Give the extent of all Plasmodium ovale-infected red blood cells.
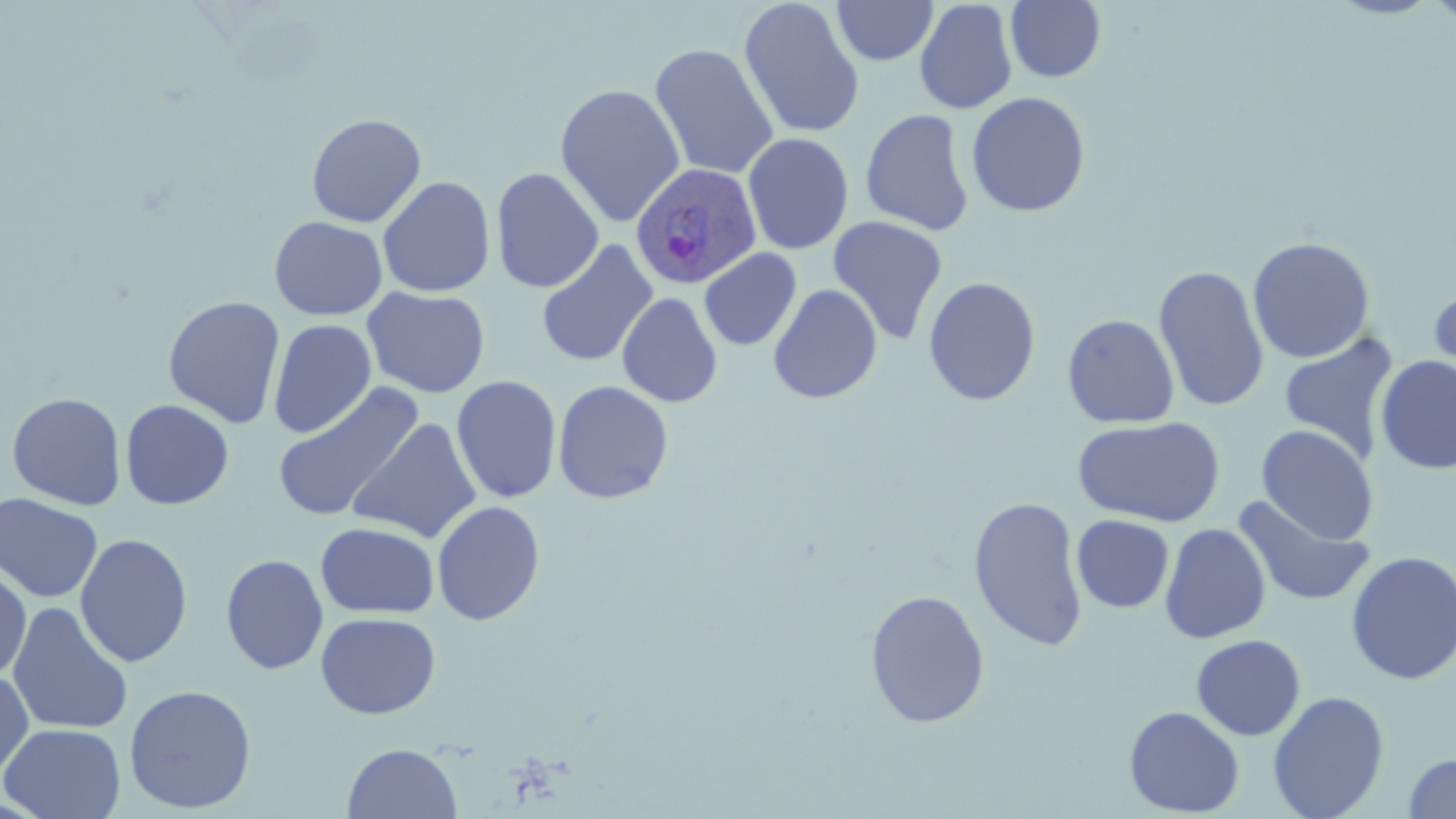

Approximate bounding boxes as (x1, y1, x2, y2) in pixels.
Plasmodium ovale-infected red blood cells: (629, 162, 763, 289).

{
  "slide_level_diagnosis": "Plasmodium ovale",
  "stain": "May-Grünwald-Giemsa",
  "field_of_view": "one of a larger specimen",
  "modality": "light microscopy",
  "image_size": "1456×819 pixels",
  "preparation": "thin blood smear",
  "magnification": "1000x",
  "uninfected_red_blood_cell_locations": "approximate bounding boxes as (x1, y1, x2, y2) in pixels: (739, 0, 865, 139), (831, 0, 938, 66), (914, 0, 1019, 115), (1328, 0, 1444, 19), (1426, 0, 1456, 28), (1004, 1, 1107, 83), (649, 43, 779, 180), (554, 83, 686, 227), (966, 91, 1090, 218), (860, 109, 975, 236), (306, 113, 427, 228), (741, 132, 854, 255), (490, 167, 604, 293), (377, 176, 496, 298), (269, 215, 388, 321), (828, 215, 949, 345), (1246, 236, 1376, 364), (536, 239, 658, 368), (699, 248, 802, 351), (1153, 264, 1270, 413), (923, 276, 1041, 406), (1426, 280, 1456, 400), (767, 283, 883, 404), (362, 286, 490, 398), (617, 292, 723, 408), (162, 295, 286, 429), (1062, 313, 1180, 429), (268, 318, 377, 439), (1278, 332, 1400, 464), (1374, 355, 1456, 474), (451, 375, 562, 504), (553, 380, 674, 504), (272, 382, 424, 524), (6, 391, 128, 510), (120, 399, 234, 509), (1072, 415, 1226, 527), (347, 417, 482, 543), (1256, 424, 1379, 544), (0, 493, 103, 603), (1232, 495, 1377, 608), (968, 496, 1088, 652), (432, 501, 545, 626), (1071, 515, 1175, 613), (316, 522, 440, 619), (1160, 522, 1271, 644), (74, 533, 193, 668), (1345, 550, 1456, 686), (221, 553, 329, 675), (0, 564, 32, 682), (865, 589, 990, 728), (7, 601, 133, 735), (315, 612, 441, 719), (1191, 634, 1306, 741), (0, 668, 34, 780), (123, 684, 256, 813), (1267, 690, 1390, 819), (1123, 706, 1245, 817), (0, 722, 127, 818), (342, 742, 463, 818), (1402, 753, 1456, 818)"
}